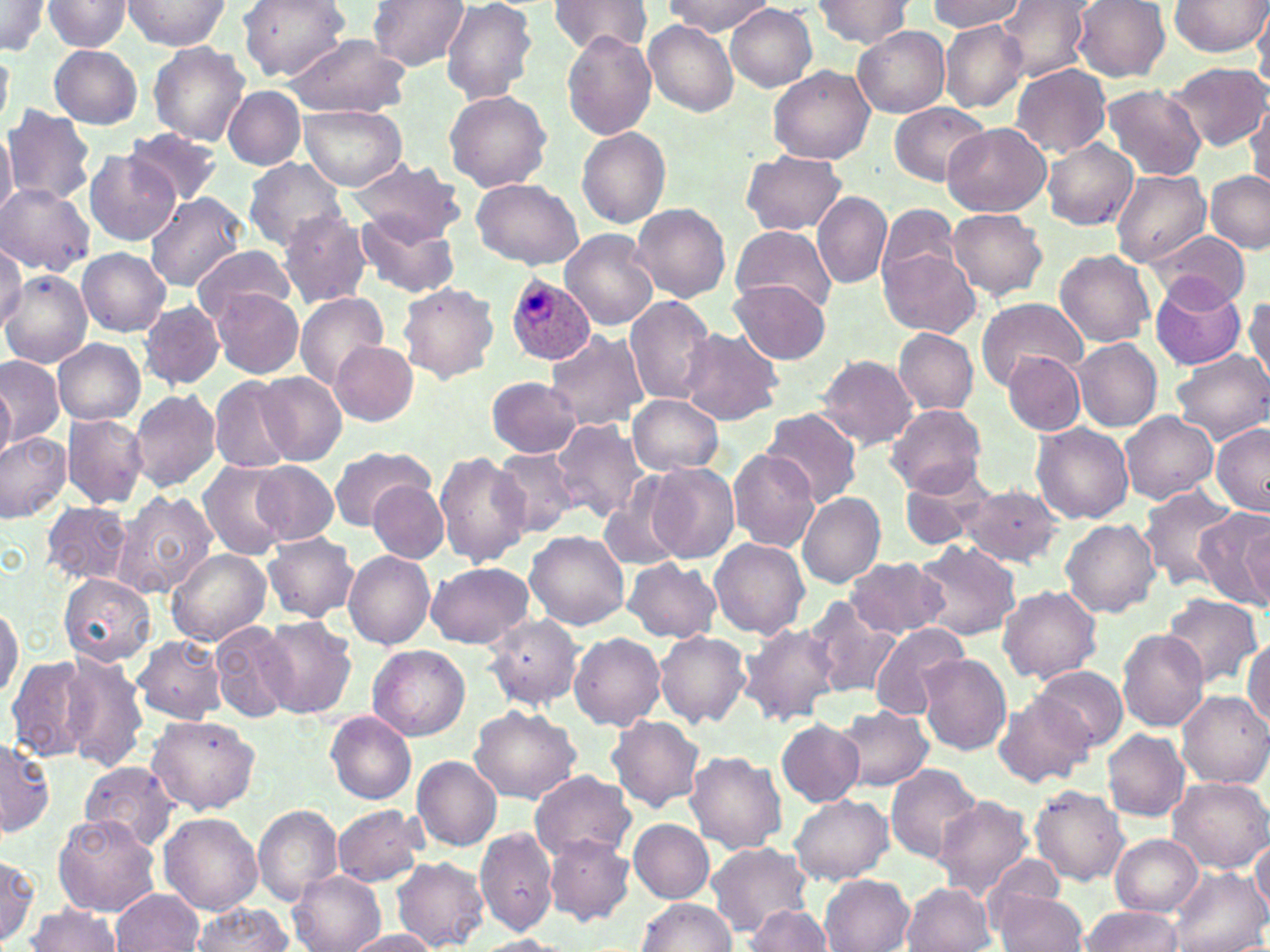
slide-level diagnosis = Plasmodium ovale
modality = light microscopy
preparation = thin blood smear
field of view = one of a larger specimen
image size = 1270×952 pixels
stain = May-Grünwald-Giemsa
Plasmodium ovale-infected red blood cell locations = approximate bounding boxes as (x1,y1)-(x2,y2) corner pairs in pixels: (506,275)-(595,365)
magnification = 1000x
uninfected red blood cell locations = approximate bounding boxes as (x1,y1)-(x2,y2) corner pairs in pixels: (41,0)-(134,51), (123,0)-(232,50), (237,0)-(350,81), (369,0)-(468,70), (549,0)-(652,58), (810,0)-(916,48), (926,0)-(1023,32), (996,0)-(1092,81), (1169,0)-(1267,57), (441,1)-(538,105), (664,1)-(772,35), (1071,1)-(1169,82), (1072,1)-(1269,69), (0,2)-(53,55), (725,4)-(817,92), (1253,5)-(1270,86), (645,21)-(739,116), (939,22)-(1028,112), (852,24)-(950,118), (561,31)-(657,140), (285,34)-(410,118), (148,42)-(250,146), (49,43)-(143,130), (0,44)-(12,132), (1163,61)-(1268,152), (1011,64)-(1111,156), (768,65)-(874,166), (1100,83)-(1207,181), (223,86)-(305,169), (444,88)-(553,192), (1247,98)-(1270,194), (889,102)-(988,184), (300,104)-(406,190), (2,105)-(95,207), (0,123)-(16,220), (940,123)-(1051,215), (576,127)-(670,228), (124,129)-(223,205), (1041,139)-(1139,230), (84,150)-(179,245), (741,152)-(847,235), (241,158)-(347,251), (347,159)-(466,244), (1112,168)-(1211,267), (1205,170)-(1270,253), (470,178)-(584,269), (0,183)-(94,274), (145,191)-(246,292), (811,191)-(893,288), (876,201)-(960,290), (631,204)-(731,303), (278,208)-(372,309), (948,209)-(1048,299), (354,211)-(459,298), (732,225)-(838,317), (562,229)-(658,330), (1152,231)-(1249,309), (0,243)-(26,332), (193,247)-(297,327), (879,247)-(979,337), (77,248)-(171,336), (1055,248)-(1154,348), (3,271)-(90,367), (1149,277)-(1247,371), (730,279)-(830,364), (398,283)-(499,384), (210,288)-(304,378), (294,291)-(389,391), (692,293)-(815,409), (623,295)-(717,407), (977,296)-(1085,388), (1245,296)-(1270,384), (139,301)-(223,389), (676,326)-(784,425), (893,327)-(978,415), (544,329)-(648,432), (54,338)-(145,424), (1073,338)-(1161,433), (330,340)-(418,425), (1169,350)-(1270,443), (1004,351)-(1086,435), (817,354)-(919,450), (0,356)-(63,447), (256,371)-(346,465), (209,375)-(295,474), (488,377)-(582,458), (0,378)-(14,463), (129,390)-(220,492), (628,395)-(722,477), (885,403)-(986,497), (761,408)-(862,507), (1121,409)-(1219,504), (62,413)-(149,509), (550,419)-(646,522), (1031,422)-(1133,524), (1211,423)-(1270,514), (0,432)-(71,523), (326,444)-(435,530), (492,448)-(580,538), (727,449)-(820,552), (434,451)-(530,567), (199,460)-(292,560), (251,462)-(338,546), (643,463)-(738,566), (899,467)-(996,551), (369,480)-(449,562), (603,482)-(686,571), (961,485)-(1063,566), (1139,486)-(1240,591), (113,490)-(217,597), (798,493)-(886,589), (39,501)-(135,586), (1193,506)-(1270,607), (1059,518)-(1160,619), (1240,518)-(1269,607), (526,531)-(630,629), (261,533)-(358,622), (709,538)-(809,639), (914,541)-(1020,642), (166,548)-(270,646), (343,549)-(434,648), (846,556)-(947,639), (622,558)-(721,643), (426,563)-(534,649), (59,574)-(155,665), (997,586)-(1101,684), (1160,592)-(1263,690), (804,595)-(900,700), (0,599)-(23,704), (483,614)-(582,709), (258,615)-(357,718), (210,621)-(295,722), (738,623)-(840,726), (868,624)-(962,721), (1117,629)-(1210,732), (656,630)-(752,726), (569,633)-(665,730), (133,635)-(226,722), (1243,637)-(1270,729), (368,645)-(469,740), (56,653)-(151,772), (916,653)-(1011,756), (5,656)-(99,763), (1029,665)-(1128,751), (1175,690)-(1270,788), (994,691)-(1092,788), (836,705)-(932,792), (470,706)-(581,802), (326,712)-(417,804), (145,715)-(261,814), (607,715)-(705,813), (775,719)-(864,806), (1102,728)-(1190,820), (0,735)-(54,836), (686,752)-(787,852), (412,755)-(502,850), (79,761)-(181,850), (886,763)-(983,864), (530,768)-(636,864), (1168,776)-(1270,873), (1029,785)-(1129,885), (789,794)-(894,885), (935,795)-(1037,900), (332,804)-(426,886), (252,805)-(343,906), (53,812)-(160,917), (159,813)-(263,914), (629,820)-(714,902), (474,827)-(558,937), (542,833)-(634,925), (1111,834)-(1202,915), (1251,838)-(1270,915), (704,840)-(814,935), (0,853)-(40,946), (393,858)-(489,950), (1169,869)-(1268,952), (291,872)-(385,952), (818,874)-(915,951), (900,882)-(995,952), (109,890)-(202,951), (994,892)-(1087,952), (636,898)-(736,952), (23,902)-(122,952), (744,903)-(831,952), (186,905)-(297,952), (1079,905)-(1183,952), (342,929)-(441,952), (477,935)-(569,952)